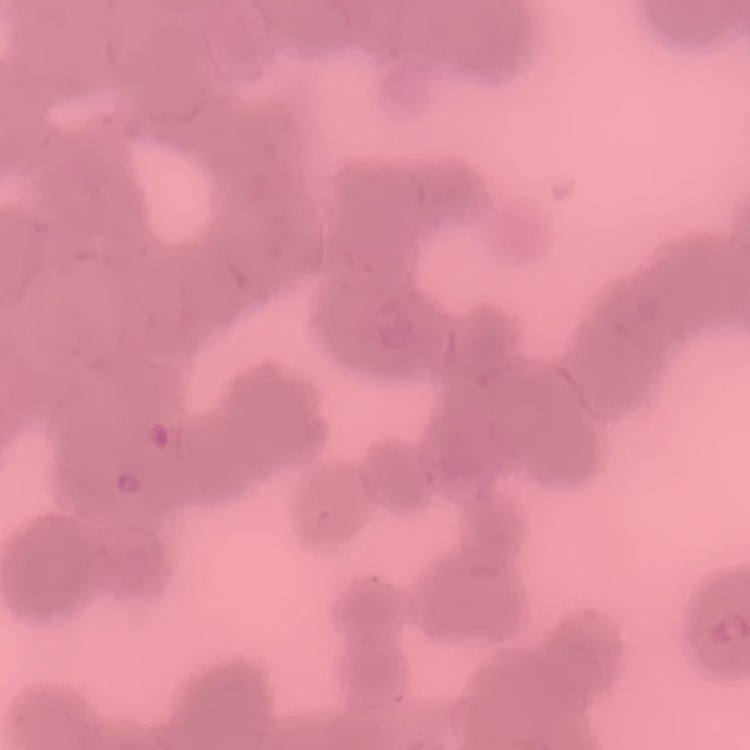

red blood cell morphology = rouleaux formation
stain = Field's or Giemsa
image type = one tile cut from a larger photomicrograph
preparation = thin blood smear